State which parasite is depicted.
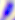
This is Toxoplasma gondii.

Micrograph. 400x magnification.